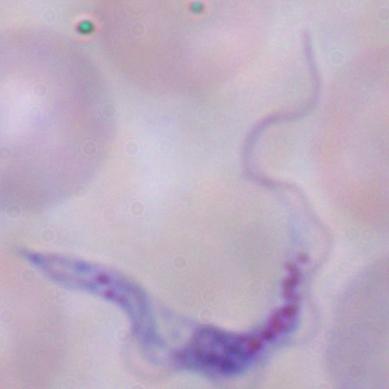
identification = trypanosome
magnification = 1000x
modality = photomicrograph